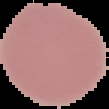
Summary:
  - Malaria status: uninfected
  - Image type: segmented cell region with the area outside set to black
  - Preparation: thin blood film
  - Image size: 109×109 pixels